Locate and identify every blood parasite.
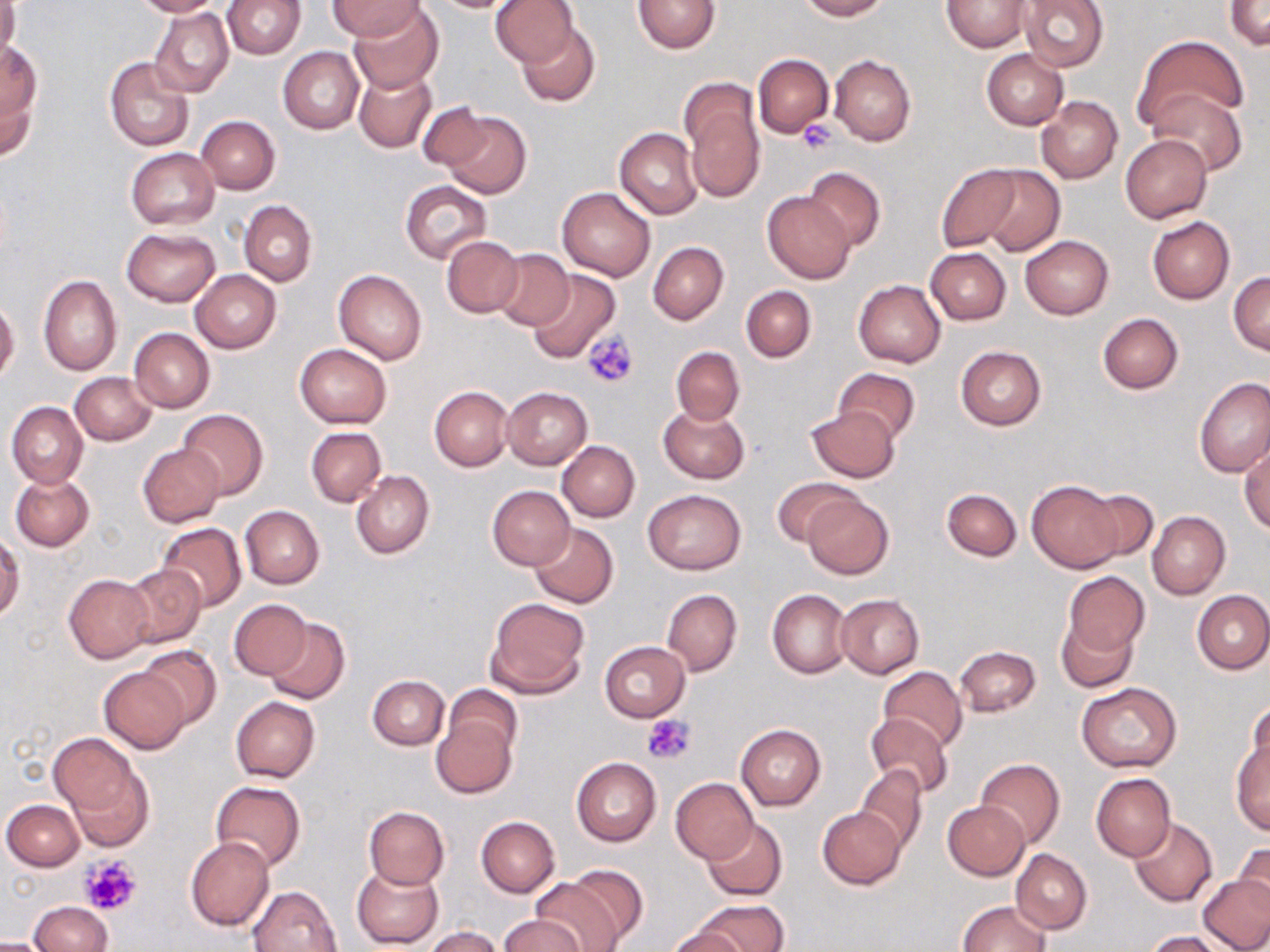
No blood parasites observed.

Summary:
  - Coordinate format: approximate bounding boxes as [x1, y1, x2, y2] in pixels
  - Platelet locations: [797, 118, 841, 152], [584, 329, 640, 389], [641, 714, 694, 765], [80, 854, 142, 916]
  - Uninfected red blood cell locations: [132, 0, 224, 17], [223, 0, 304, 58], [490, 0, 579, 67], [634, 0, 720, 54], [797, 0, 889, 20], [942, 0, 1033, 51], [1017, 0, 1108, 72], [1225, 0, 1270, 50], [0, 1, 19, 64], [329, 1, 423, 40], [423, 1, 522, 13], [349, 4, 443, 93], [150, 7, 234, 97], [516, 20, 600, 106], [1135, 35, 1245, 128], [1, 40, 42, 129], [278, 47, 364, 134], [982, 49, 1067, 129], [753, 53, 835, 136], [830, 54, 916, 146], [105, 56, 195, 152], [353, 67, 437, 154], [0, 72, 39, 163], [682, 87, 766, 203], [1148, 89, 1247, 175], [1037, 97, 1122, 183], [420, 101, 491, 171], [438, 110, 532, 199], [196, 116, 280, 193], [615, 127, 703, 219], [1120, 134, 1213, 222], [125, 148, 220, 229], [935, 164, 1022, 252], [802, 165, 885, 251], [976, 165, 1064, 256], [400, 182, 491, 263], [558, 187, 655, 281], [763, 191, 856, 283], [239, 200, 317, 286], [1147, 216, 1235, 303], [122, 227, 221, 307], [1020, 236, 1113, 319], [441, 237, 524, 317], [647, 241, 728, 324], [926, 247, 1011, 324], [491, 248, 574, 330], [190, 270, 281, 353], [333, 270, 428, 365], [526, 270, 620, 362], [1229, 272, 1270, 356], [39, 275, 122, 375], [853, 280, 945, 367], [740, 284, 816, 362], [0, 300, 20, 383], [1097, 313, 1184, 395], [129, 328, 214, 412], [295, 343, 392, 428], [671, 345, 745, 426], [955, 345, 1046, 429], [832, 367, 921, 445], [70, 372, 156, 445], [1195, 377, 1270, 477], [430, 386, 513, 472], [502, 387, 592, 470], [7, 401, 88, 487], [659, 404, 749, 484], [807, 406, 900, 482], [178, 410, 268, 501], [306, 427, 386, 506], [557, 440, 640, 522], [1240, 441, 1269, 534], [138, 443, 224, 526], [351, 469, 434, 559], [10, 473, 94, 551], [773, 476, 860, 547], [1026, 480, 1122, 572], [487, 485, 576, 570], [941, 487, 1021, 562], [1083, 488, 1159, 564], [642, 489, 747, 574], [803, 492, 893, 579], [240, 505, 324, 589], [1147, 511, 1230, 599], [155, 523, 246, 612], [530, 523, 619, 609], [0, 533, 23, 622], [121, 564, 205, 648], [1063, 572, 1149, 655], [64, 573, 155, 663], [662, 589, 742, 676], [767, 589, 851, 678], [1192, 590, 1270, 674], [835, 594, 924, 678], [485, 596, 590, 699], [229, 599, 312, 679], [1056, 617, 1137, 691], [265, 618, 350, 705], [599, 641, 690, 722], [136, 644, 220, 728], [955, 645, 1041, 717], [877, 666, 968, 754], [100, 667, 190, 753], [368, 675, 449, 750], [1077, 681, 1182, 772], [443, 684, 522, 762], [230, 696, 320, 782], [1243, 704, 1268, 788], [865, 712, 954, 799], [432, 715, 516, 800], [735, 723, 825, 810], [51, 734, 154, 849], [1231, 737, 1269, 835], [571, 757, 661, 847], [975, 758, 1064, 850], [856, 765, 926, 855], [1091, 772, 1177, 861], [671, 778, 759, 864], [210, 781, 305, 872], [195, 783, 296, 940], [2, 799, 84, 871], [943, 800, 1029, 879], [363, 806, 449, 889], [817, 808, 904, 889], [476, 816, 560, 897], [1129, 817, 1219, 907], [701, 819, 787, 900], [185, 837, 274, 931], [1234, 840, 1269, 916], [1012, 849, 1091, 935], [351, 864, 443, 947], [564, 864, 649, 946], [1199, 872, 1269, 952], [530, 875, 626, 952], [249, 884, 344, 952], [27, 901, 114, 951], [692, 901, 787, 952], [957, 901, 1049, 952], [501, 913, 584, 952], [423, 926, 504, 952], [664, 927, 744, 952], [1145, 931, 1227, 952]
  - Slide-level diagnosis: no evidence of blood parasites
  - Magnification: 1000x
  - Image size: 1270×952 pixels
  - Modality: light microscopy
  - Field of view: single
  - Preparation: thin blood smear
  - Stain: May-Grünwald-Giemsa